Name the cell type shown.
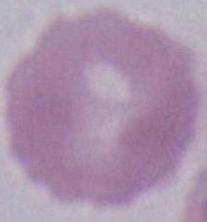
This is an erythrocyte.

magnification = 1000x
modality = photomicrograph